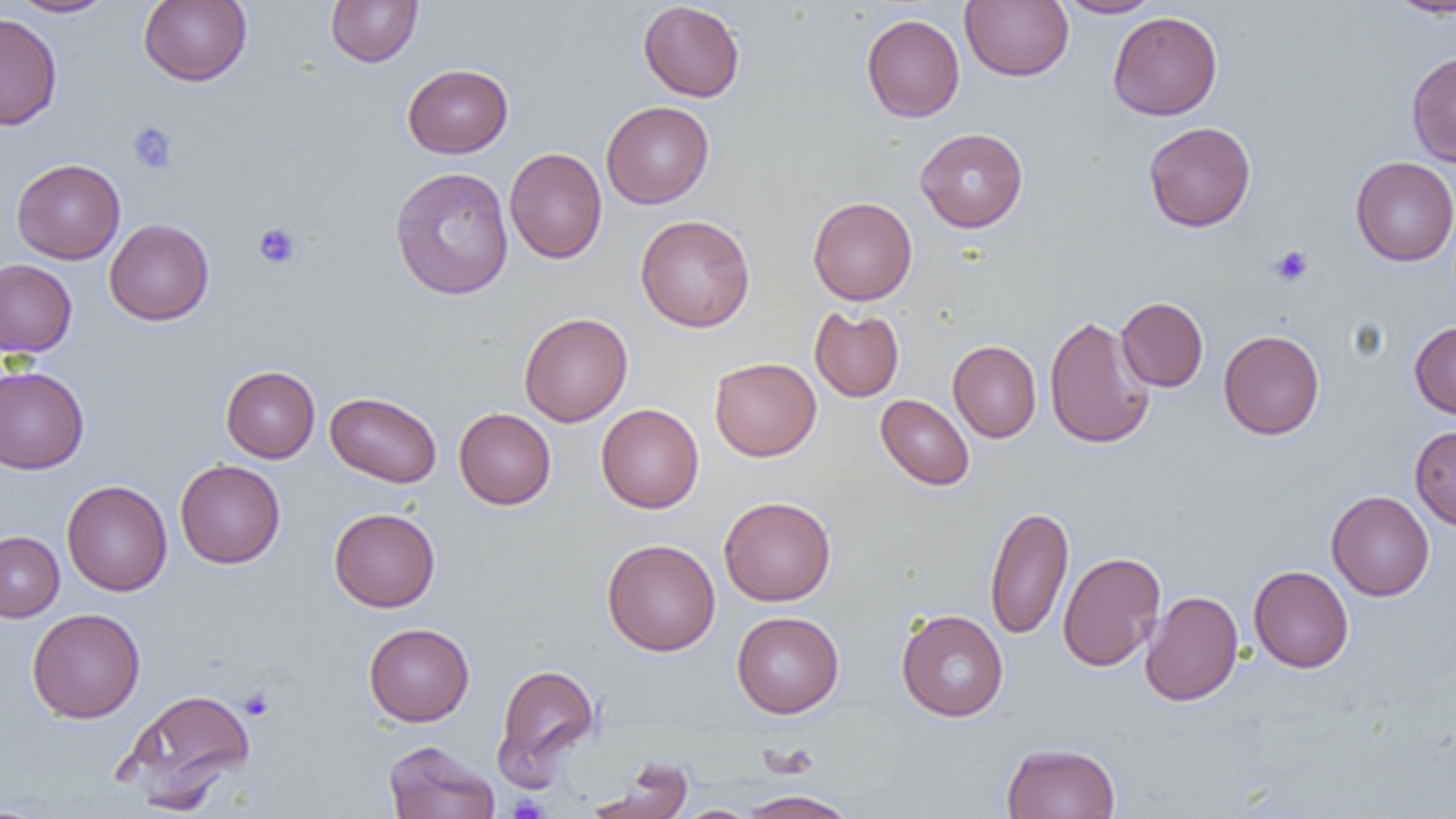

Approximate bounding boxes as (x1, y1, x2, y2) in pixels. Uninfected red blood cell locations: (9, 0, 117, 17), (138, 0, 252, 86), (325, 0, 423, 67), (960, 0, 1073, 81), (1057, 0, 1163, 18), (1385, 0, 1456, 18), (638, 1, 745, 102), (1107, 11, 1223, 120), (0, 12, 62, 131), (861, 14, 964, 122), (1406, 51, 1456, 167), (403, 64, 513, 158), (601, 101, 714, 208), (1143, 121, 1256, 232), (915, 128, 1028, 232), (505, 148, 607, 264), (1350, 156, 1456, 266), (11, 159, 125, 264), (389, 166, 514, 299), (807, 196, 918, 305), (635, 214, 756, 332), (104, 219, 214, 325), (0, 259, 77, 357), (1116, 297, 1208, 392), (809, 306, 904, 402), (519, 312, 633, 426), (1044, 314, 1155, 449), (1409, 322, 1456, 419), (1218, 329, 1325, 440), (948, 341, 1041, 442), (709, 357, 821, 461), (221, 365, 320, 463), (0, 366, 89, 474), (325, 392, 442, 487), (876, 394, 974, 490), (596, 403, 704, 513), (454, 408, 556, 509), (1410, 425, 1456, 531), (175, 459, 285, 568), (62, 480, 172, 596), (1326, 490, 1434, 601), (719, 495, 836, 606), (985, 505, 1073, 640), (329, 507, 440, 612), (0, 531, 64, 622), (601, 538, 720, 655), (1057, 551, 1166, 672), (1249, 565, 1354, 673), (1140, 591, 1243, 706), (27, 607, 145, 723), (896, 609, 1008, 721), (731, 611, 844, 718), (363, 622, 475, 726), (492, 663, 600, 785), (118, 688, 256, 810), (383, 740, 500, 819), (1001, 742, 1121, 819), (587, 758, 693, 819), (738, 789, 860, 818), (0, 803, 52, 818), (674, 805, 758, 818). Platelet locations: (128, 121, 179, 174), (253, 222, 302, 269), (1268, 245, 1313, 287), (240, 687, 275, 720), (506, 794, 550, 819). Slide-level diagnosis: no evidence of blood parasites. One field of a larger specimen. Thin blood smear. Image is 1456×819 pixels. 1000x magnification. Light microscopy.